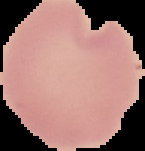

Malaria status: uninfected. From a thin blood smear. The area outside the segmented cell region is set to black. Image is 145×151 pixels.